Assess the morphology of the red blood cells.
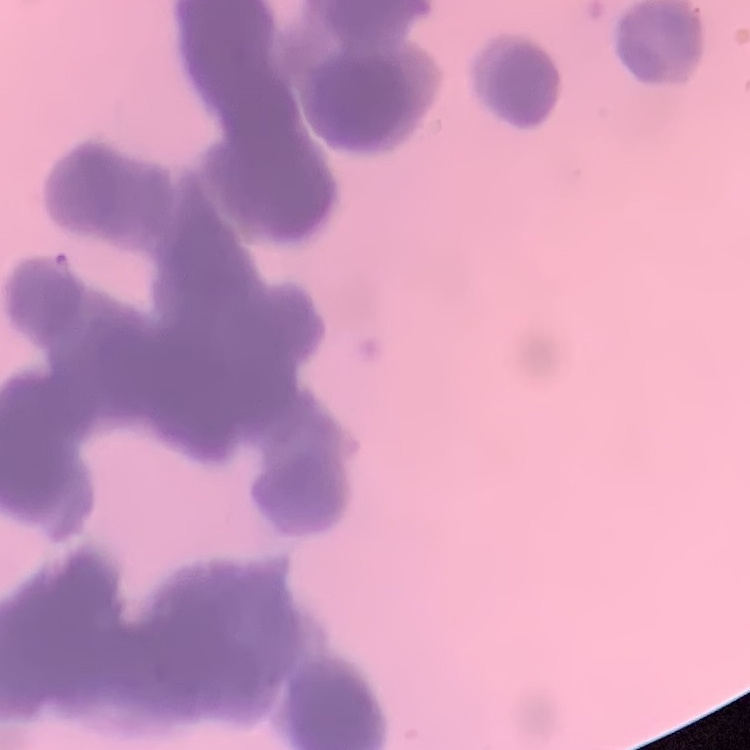

Rouleaux formation.

Stained with either Field's or Giemsa. One tile cut from a larger photomicrograph. Thin blood film.